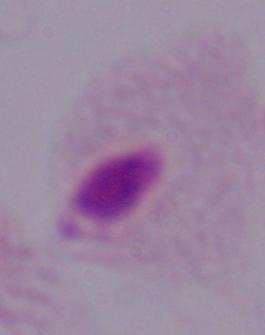

1000x magnification. Micrograph. A trichomonad is seen.